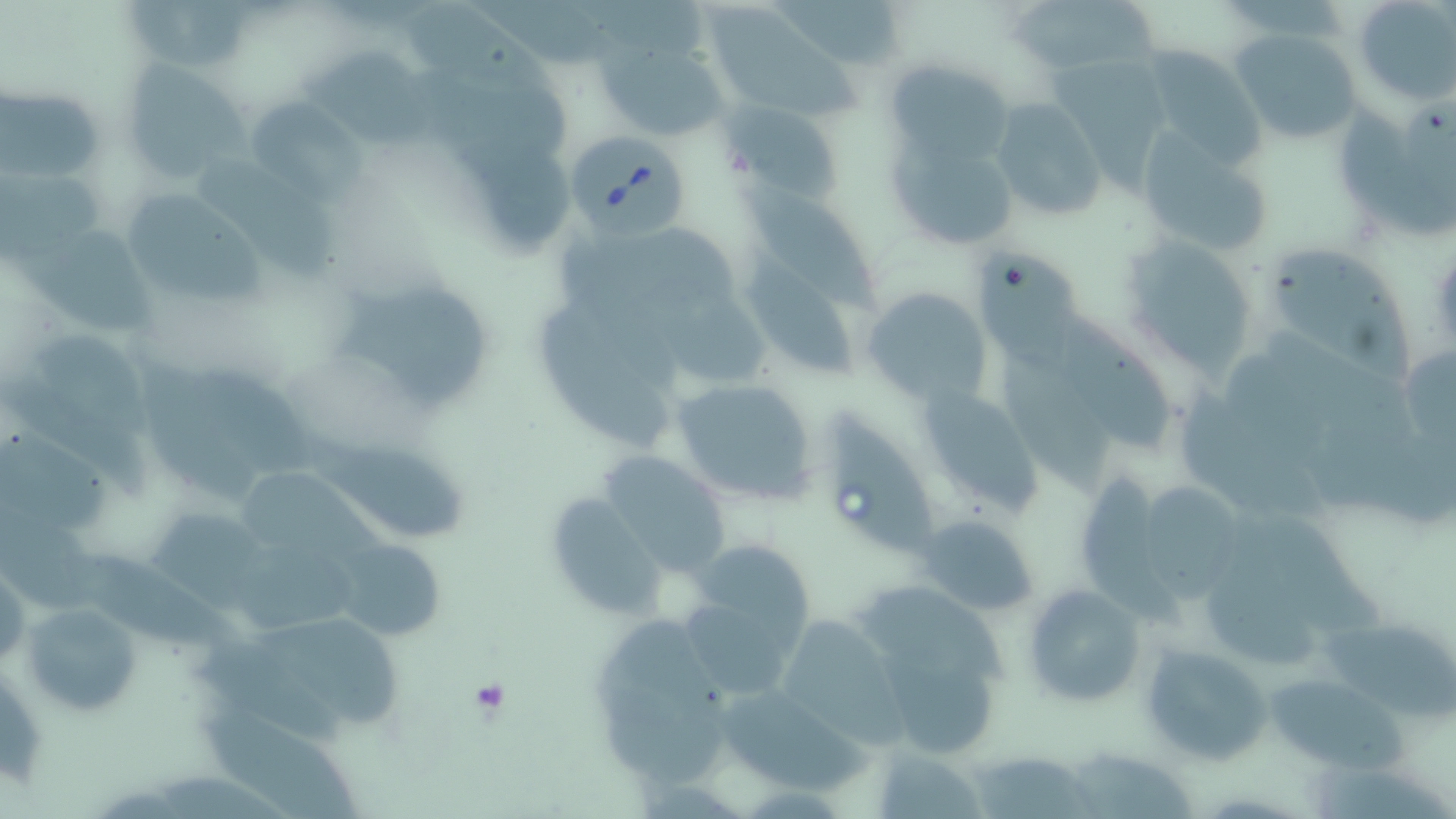
slide-level diagnosis = Babesia divergens
platelet locations = approximate bounding boxes as (x1, y1, x2, y2) in pixels: (466, 680, 512, 717)
stain = May-Grünwald-Giemsa
uninfected red blood cell locations = approximate bounding boxes as (x1, y1, x2, y2) in pixels: (1006, 0, 1162, 82), (1352, 0, 1455, 104), (704, 6, 863, 117), (1230, 28, 1363, 148), (594, 35, 729, 143), (1132, 43, 1269, 167), (309, 52, 458, 148), (1050, 55, 1176, 200), (118, 59, 251, 184), (424, 64, 580, 163), (892, 66, 1009, 158), (1, 85, 105, 184), (248, 96, 361, 198), (991, 98, 1107, 225), (725, 102, 845, 205), (1341, 104, 1453, 235), (1136, 129, 1275, 261), (892, 134, 1012, 245), (200, 148, 336, 277), (1, 163, 105, 261), (741, 179, 883, 320), (118, 186, 266, 306), (24, 227, 160, 332), (1121, 235, 1263, 380), (1260, 242, 1408, 379), (742, 249, 853, 374), (979, 249, 1086, 382), (338, 277, 495, 408), (863, 287, 991, 407), (538, 300, 670, 449), (1057, 308, 1174, 446), (23, 323, 155, 438), (173, 357, 324, 473), (1003, 357, 1113, 492), (670, 377, 819, 508), (920, 381, 1041, 513), (1182, 381, 1334, 517), (828, 410, 944, 562), (313, 434, 467, 547), (0, 435, 117, 530), (598, 450, 735, 575), (1080, 470, 1184, 630), (1141, 478, 1246, 600), (552, 497, 663, 617), (145, 503, 274, 608), (1231, 507, 1383, 641), (917, 514, 1039, 615), (334, 539, 445, 640), (220, 541, 370, 625), (696, 543, 815, 658), (60, 548, 243, 656), (0, 561, 27, 670), (1204, 565, 1319, 666), (862, 577, 1009, 679), (1022, 582, 1144, 708), (21, 600, 143, 715), (1326, 610, 1456, 721), (772, 613, 905, 745), (247, 614, 407, 729), (1139, 641, 1273, 766), (877, 651, 1002, 754), (1259, 673, 1402, 767), (707, 684, 875, 797), (206, 710, 366, 818), (872, 744, 979, 819), (1061, 745, 1201, 818), (969, 747, 1098, 819)
field of view = single
magnification = 1000x
image size = 1456×819 pixels
modality = light microscopy
Babesia divergens-infected red blood cell locations = approximate bounding boxes as (x1, y1, x2, y2) in pixels: (571, 131, 686, 238)
preparation = thin blood film